Identify the parasite.
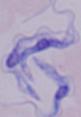

A trypanosome.

modality = photomicrograph
magnification = 1000x